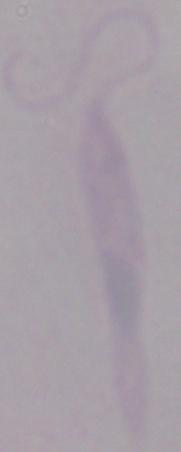

Summary:
  - Modality: photomicrograph
  - Identification: Leishmania
  - Magnification: 1000x